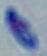

Summary:
  - Modality: micrograph
  - Identification: Toxoplasma gondii
  - Magnification: 1000x